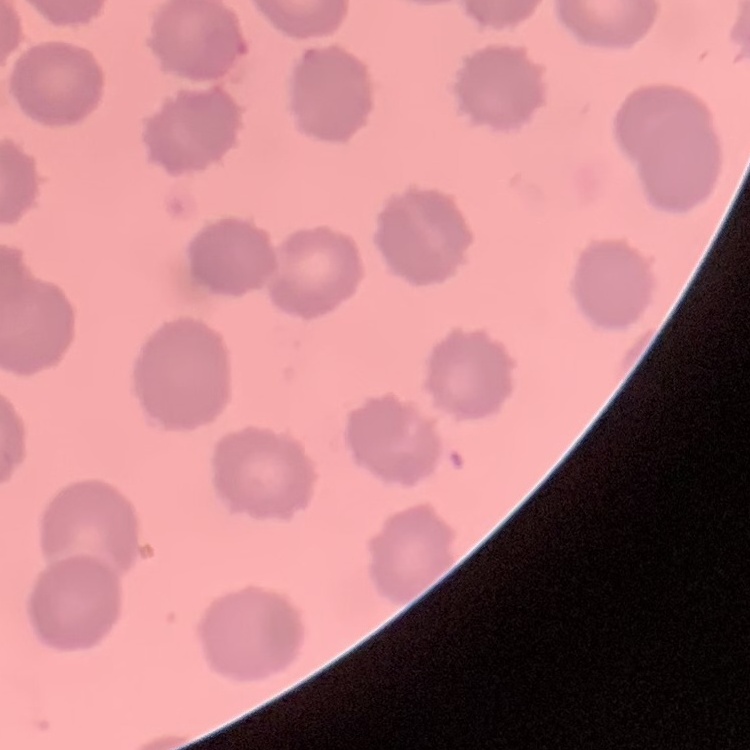
Summary:
  - Red blood cell morphology: no rouleaux formation
  - Preparation: thin blood film
  - Stain: Field's or Giemsa
  - Image type: one tile cut from a larger photomicrograph